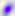
Photomicrograph. Captured at 400x magnification. Toxoplasma gondii is seen.